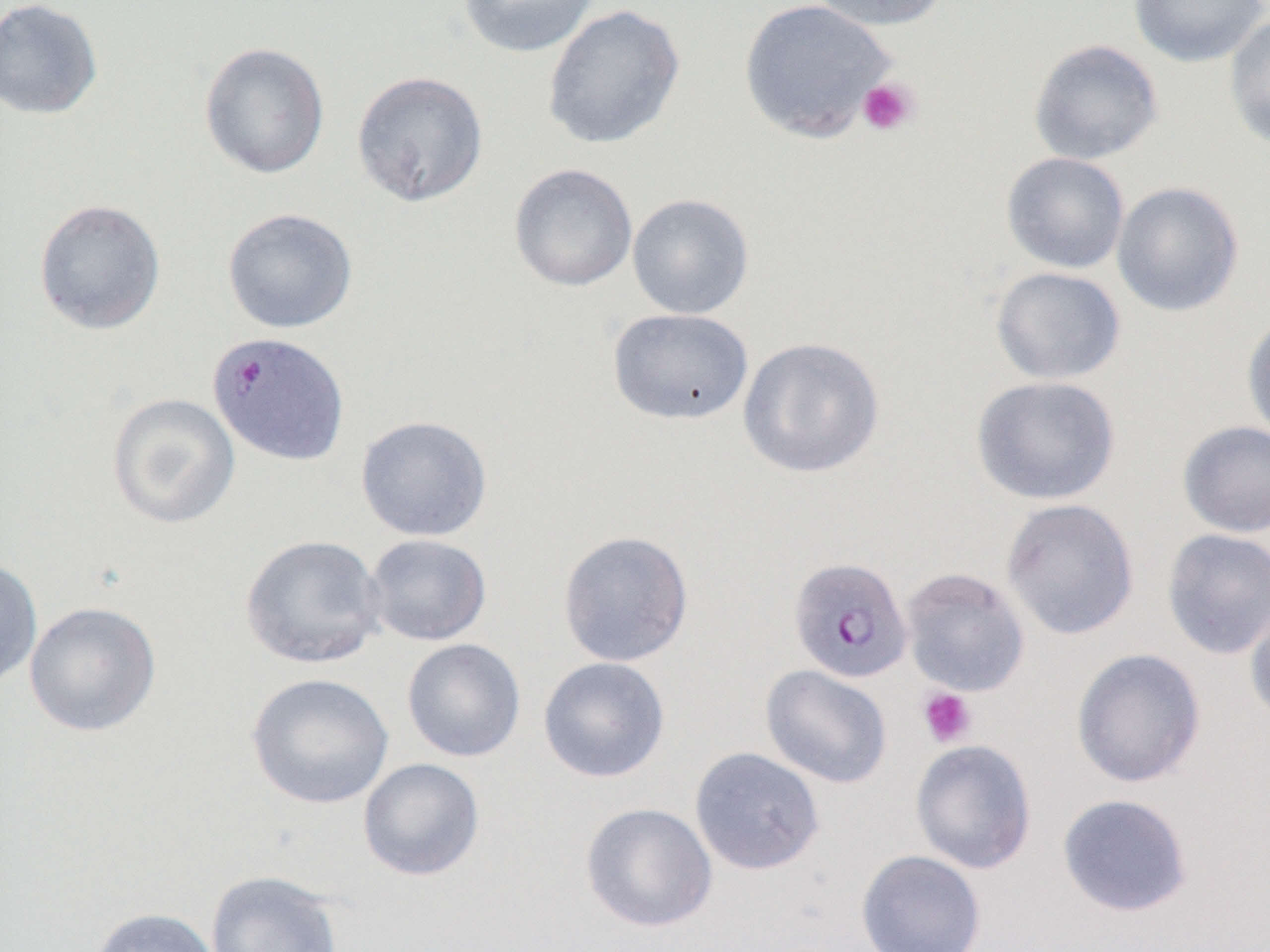 Approximate bounding boxes as [x1, y1, x2, y2] in pixels. Platelet locations: [857, 76, 920, 136], [917, 687, 977, 747]. Uninfected red blood cell locations: [0, 0, 103, 120], [457, 0, 600, 58], [738, 0, 898, 143], [806, 0, 951, 32], [1128, 0, 1270, 68], [542, 4, 685, 150], [1223, 11, 1270, 151], [1029, 39, 1164, 165], [198, 41, 331, 180], [351, 70, 489, 207], [1002, 152, 1130, 274], [508, 162, 638, 292], [1112, 181, 1244, 317], [626, 192, 754, 319], [33, 199, 166, 335], [222, 207, 358, 334], [990, 266, 1126, 385], [607, 308, 754, 426], [1241, 312, 1270, 445], [737, 336, 886, 479], [971, 375, 1120, 505], [106, 392, 241, 529], [355, 415, 493, 542], [1177, 420, 1270, 538], [1001, 498, 1139, 640], [1161, 528, 1270, 660], [557, 530, 694, 667], [363, 533, 493, 647], [240, 534, 386, 669], [0, 556, 43, 689], [900, 567, 1030, 696], [1244, 591, 1270, 729], [24, 601, 162, 737], [401, 638, 526, 762], [1071, 648, 1206, 788], [538, 656, 670, 783], [760, 664, 892, 789], [247, 672, 394, 809], [910, 738, 1037, 874], [689, 746, 825, 876], [358, 757, 485, 881], [1057, 793, 1194, 917], [580, 802, 718, 932], [856, 849, 986, 952], [205, 870, 343, 952], [87, 906, 221, 952]. Plasmodium falciparum-infected red blood cell locations: [206, 330, 351, 467], [788, 556, 913, 683]. Slide-level diagnosis: Plasmodium falciparum. Optical microscopy. Image is 1270×952 pixels. Single field of view. Captured at 1000x magnification. Thin blood film.